State which parasite is depicted.
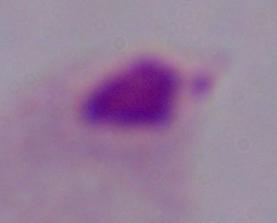

A trichomonad.

1000x magnification. Micrograph.